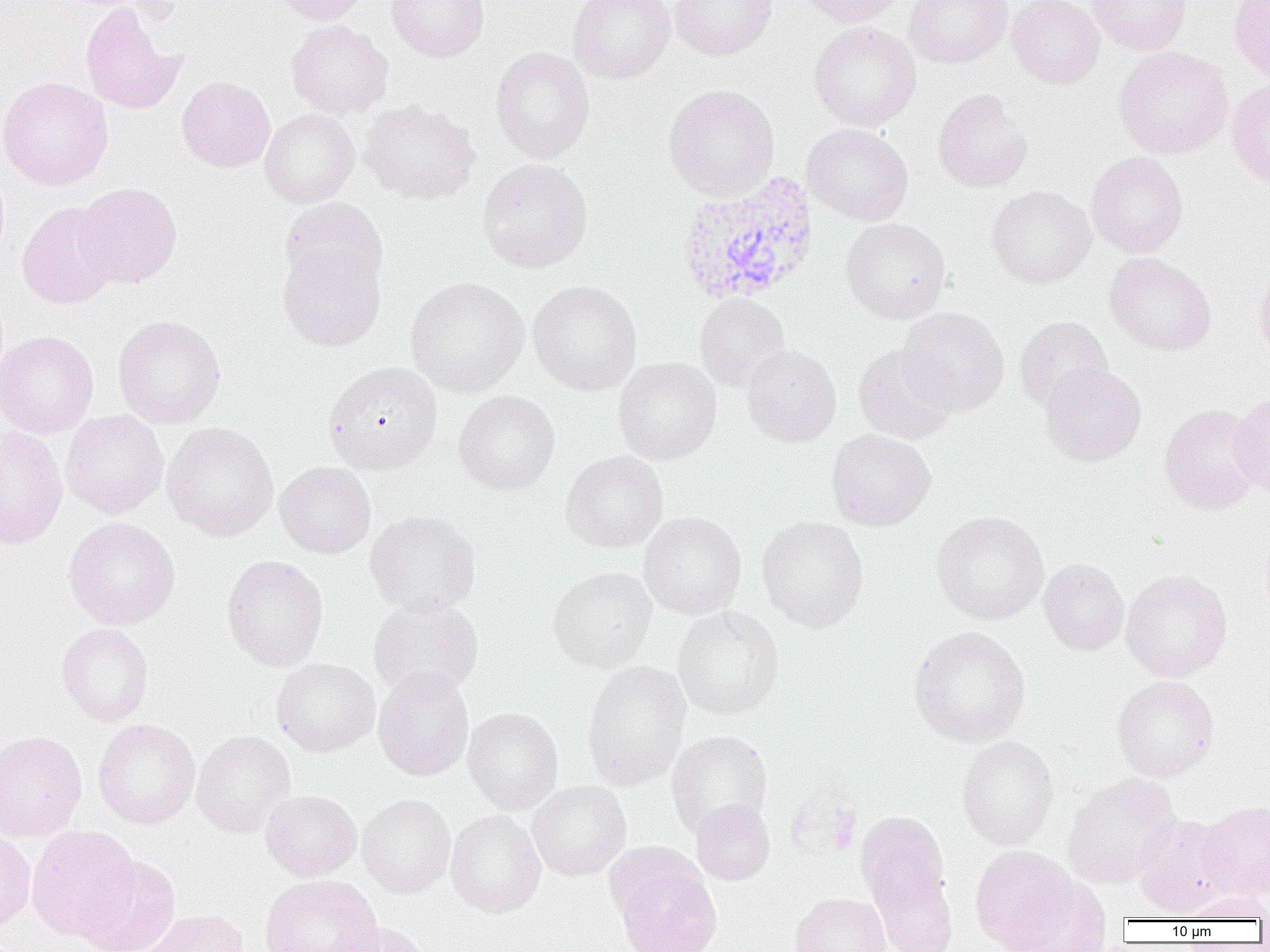 Approximate bounding boxes as [x1, y1, x2, y2] in pixels. Plasmodium vivax-infected red blood cell locations: [675, 172, 819, 307]. Uninfected red blood cell locations: [273, 0, 370, 26], [385, 0, 490, 62], [568, 0, 675, 83], [670, 0, 777, 60], [795, 0, 907, 27], [904, 0, 1013, 69], [1007, 0, 1104, 89], [1087, 0, 1191, 55], [1229, 0, 1270, 83], [80, 1, 188, 115], [285, 20, 393, 118], [809, 21, 921, 132], [490, 47, 594, 163], [1113, 47, 1233, 159], [177, 76, 275, 173], [0, 77, 113, 190], [1226, 78, 1270, 187], [663, 84, 780, 201], [932, 88, 1034, 192], [359, 99, 481, 205], [259, 108, 360, 208], [802, 123, 913, 226], [1086, 152, 1188, 257], [477, 159, 593, 273], [74, 182, 182, 288], [987, 186, 1096, 288], [279, 197, 388, 295], [17, 200, 121, 308], [840, 218, 951, 324], [277, 240, 386, 352], [1104, 252, 1216, 355], [1253, 262, 1270, 362], [405, 276, 529, 397], [528, 280, 642, 395], [694, 293, 790, 391], [896, 307, 1009, 415], [113, 315, 226, 428], [1014, 315, 1112, 413], [0, 331, 99, 439], [853, 343, 957, 445], [742, 345, 841, 447], [613, 356, 722, 466], [323, 361, 442, 474], [1040, 363, 1146, 467], [453, 390, 560, 496], [1230, 392, 1270, 501], [1159, 402, 1264, 515], [60, 410, 168, 519], [162, 422, 279, 541], [0, 425, 68, 549], [826, 428, 935, 532], [560, 450, 669, 553], [274, 461, 376, 559], [365, 510, 481, 616], [638, 511, 746, 620], [930, 511, 1049, 625], [756, 515, 869, 632], [63, 517, 180, 630], [221, 555, 329, 671], [1038, 558, 1129, 656], [548, 566, 656, 672], [1121, 569, 1232, 681], [368, 595, 484, 699], [672, 606, 784, 720], [56, 623, 154, 726], [907, 626, 1030, 747], [271, 657, 380, 757], [581, 660, 692, 791], [373, 666, 474, 781], [1112, 675, 1219, 782], [462, 707, 564, 814], [93, 718, 201, 829], [0, 730, 87, 841], [192, 730, 296, 838], [666, 730, 772, 839], [956, 735, 1059, 850], [1062, 773, 1181, 888], [526, 780, 631, 881], [260, 789, 362, 881], [356, 793, 456, 898], [691, 799, 775, 885], [1198, 801, 1270, 900], [446, 810, 546, 918], [856, 810, 953, 935], [1133, 814, 1237, 918], [26, 825, 141, 942], [0, 828, 36, 934], [971, 845, 1079, 950], [78, 856, 181, 952], [615, 863, 722, 952], [259, 874, 383, 952], [1005, 877, 1112, 952], [1176, 891, 1270, 922], [790, 892, 891, 951], [135, 907, 251, 952], [327, 921, 433, 952]. Slide-level diagnosis: Plasmodium vivax. 1000x magnification. Thin blood smear. Light microscopy. Single field of view. Image is 1270×952 pixels.